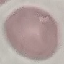

{
  "result": "no malaria parasites detected",
  "stain": "Giemsa",
  "image_type": "automatically extracted cell patch, resized to 64 × 64 pixels",
  "capture": "smartphone camera at the microscope eyepiece",
  "preparation": "thin blood film"
}